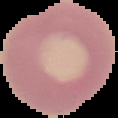

Summary:
  - Image size: 118×118 pixels
  - Preparation: thin blood film
  - Image type: segmented cell region with the area outside set to black
  - Malaria status: uninfected